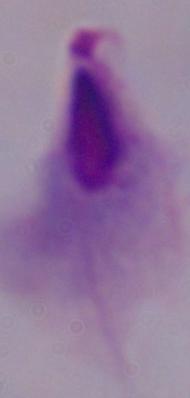

Summary:
  - Modality: photomicrograph
  - Magnification: 1000x
  - Identification: trichomonad